Outline each Plasmodium falciparum-infected red blood cell.
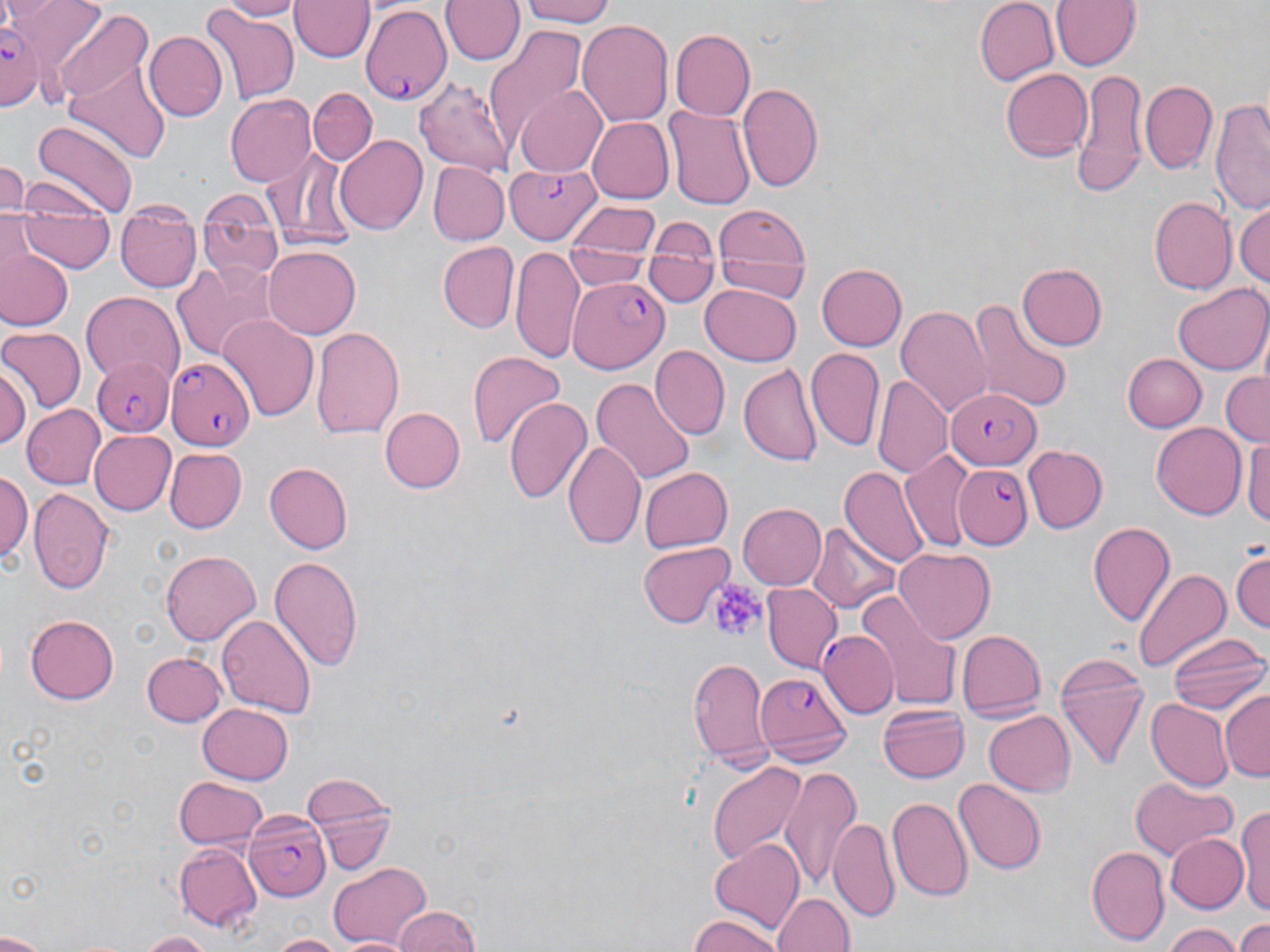
Approximate bounding boxes as [x1, y1, x2, y2] in pixels.
Plasmodium falciparum-infected red blood cells: [357, 6, 451, 104], [1, 20, 44, 108], [504, 163, 601, 244], [567, 276, 666, 368], [90, 355, 175, 437], [168, 358, 256, 452], [945, 387, 1040, 469], [955, 461, 1033, 549], [819, 630, 897, 718], [756, 669, 850, 760], [244, 809, 333, 902].

Platelet locations: [708, 580, 767, 644]. Uninfected red blood cell locations: [11, 0, 107, 82], [214, 0, 304, 21], [442, 0, 524, 66], [515, 0, 621, 26], [976, 0, 1059, 85], [1047, 0, 1143, 71], [291, 1, 373, 63], [198, 6, 299, 105], [54, 9, 153, 113], [578, 17, 675, 130], [484, 23, 587, 143], [670, 29, 754, 120], [143, 30, 226, 121], [64, 51, 171, 163], [1002, 70, 1092, 159], [1070, 71, 1150, 198], [416, 78, 517, 174], [1140, 80, 1217, 175], [740, 82, 824, 193], [515, 86, 608, 176], [308, 87, 376, 164], [225, 95, 315, 185], [1211, 99, 1269, 214], [665, 105, 755, 210], [586, 116, 672, 204], [31, 120, 139, 219], [334, 135, 431, 235], [262, 148, 359, 253], [0, 160, 28, 213], [427, 161, 510, 246], [199, 189, 283, 282], [1151, 196, 1236, 294], [1235, 201, 1269, 292], [567, 202, 660, 261], [710, 204, 810, 275], [117, 208, 203, 293], [18, 217, 116, 273], [649, 219, 718, 263], [713, 233, 810, 300], [437, 242, 516, 334], [512, 242, 585, 368], [564, 243, 654, 290], [262, 246, 361, 339], [2, 249, 72, 329], [645, 252, 716, 306], [171, 258, 285, 363], [1015, 261, 1106, 352], [817, 264, 908, 352], [701, 284, 801, 364], [1172, 285, 1270, 374], [81, 293, 186, 389], [968, 300, 1073, 413], [897, 305, 992, 422], [220, 317, 318, 421], [310, 324, 404, 440], [1, 325, 85, 414], [650, 346, 730, 441], [465, 348, 566, 450], [805, 348, 885, 451], [1121, 353, 1207, 432], [1, 363, 30, 448], [738, 363, 822, 468], [1219, 370, 1270, 448], [875, 374, 953, 478], [591, 375, 694, 483], [505, 396, 593, 506], [23, 404, 104, 490], [380, 408, 465, 493], [1151, 423, 1245, 520], [87, 430, 176, 516], [1243, 435, 1270, 534], [565, 438, 643, 546], [1022, 446, 1108, 533], [164, 449, 245, 531], [901, 450, 974, 549], [264, 463, 352, 554], [841, 466, 930, 570], [639, 467, 733, 552], [2, 469, 32, 569], [29, 489, 114, 595], [738, 502, 828, 591], [809, 521, 899, 615], [1087, 521, 1176, 627], [638, 543, 735, 627], [1232, 546, 1270, 633], [894, 548, 995, 643], [160, 550, 261, 647], [269, 555, 364, 670], [1134, 568, 1231, 673], [761, 583, 842, 674], [858, 592, 963, 708], [24, 613, 120, 705], [217, 615, 316, 718], [958, 628, 1045, 721], [1167, 634, 1269, 717], [141, 651, 227, 726], [1055, 652, 1147, 770], [688, 655, 772, 772], [1221, 690, 1269, 782], [1145, 697, 1230, 790], [197, 701, 293, 783], [877, 702, 971, 784], [983, 709, 1077, 796], [706, 760, 808, 867], [779, 767, 861, 891], [302, 773, 400, 875], [173, 776, 268, 850], [1131, 776, 1235, 862], [954, 779, 1047, 875], [887, 798, 971, 903], [1236, 803, 1270, 917], [830, 817, 898, 921], [1168, 834, 1246, 911], [708, 837, 803, 932], [174, 842, 260, 932], [1087, 846, 1169, 943], [327, 862, 435, 947], [773, 892, 855, 952], [395, 907, 481, 952], [684, 915, 787, 952], [1232, 917, 1270, 951], [1162, 922, 1238, 952], [0, 929, 52, 951], [138, 930, 210, 951], [266, 934, 356, 952]. Slide-level diagnosis: Plasmodium falciparum. May-Grünwald-Giemsa stain. Image is 1270×952 pixels. Light microscopy. One field of a larger specimen. Thin blood film. Captured at 1000x magnification.